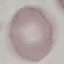
result: no malaria parasites seen
image_type: cell patch, automatically extracted from a larger field of view and resized to 64 × 64 pixels
capture: smartphone through the microscope eyepiece
preparation: thin blood film
stain: Giemsa